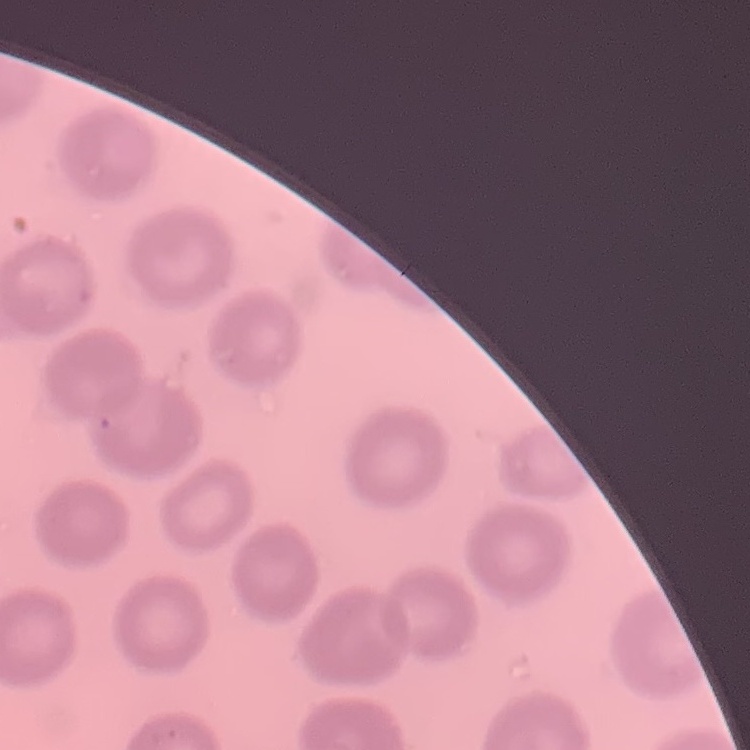
erythrocyte morphology = no rouleaux formation
preparation = thin peripheral smear
stain = Field's or Giemsa
image type = one tile cut from a larger photomicrograph